Look for Plasmodium parasites.
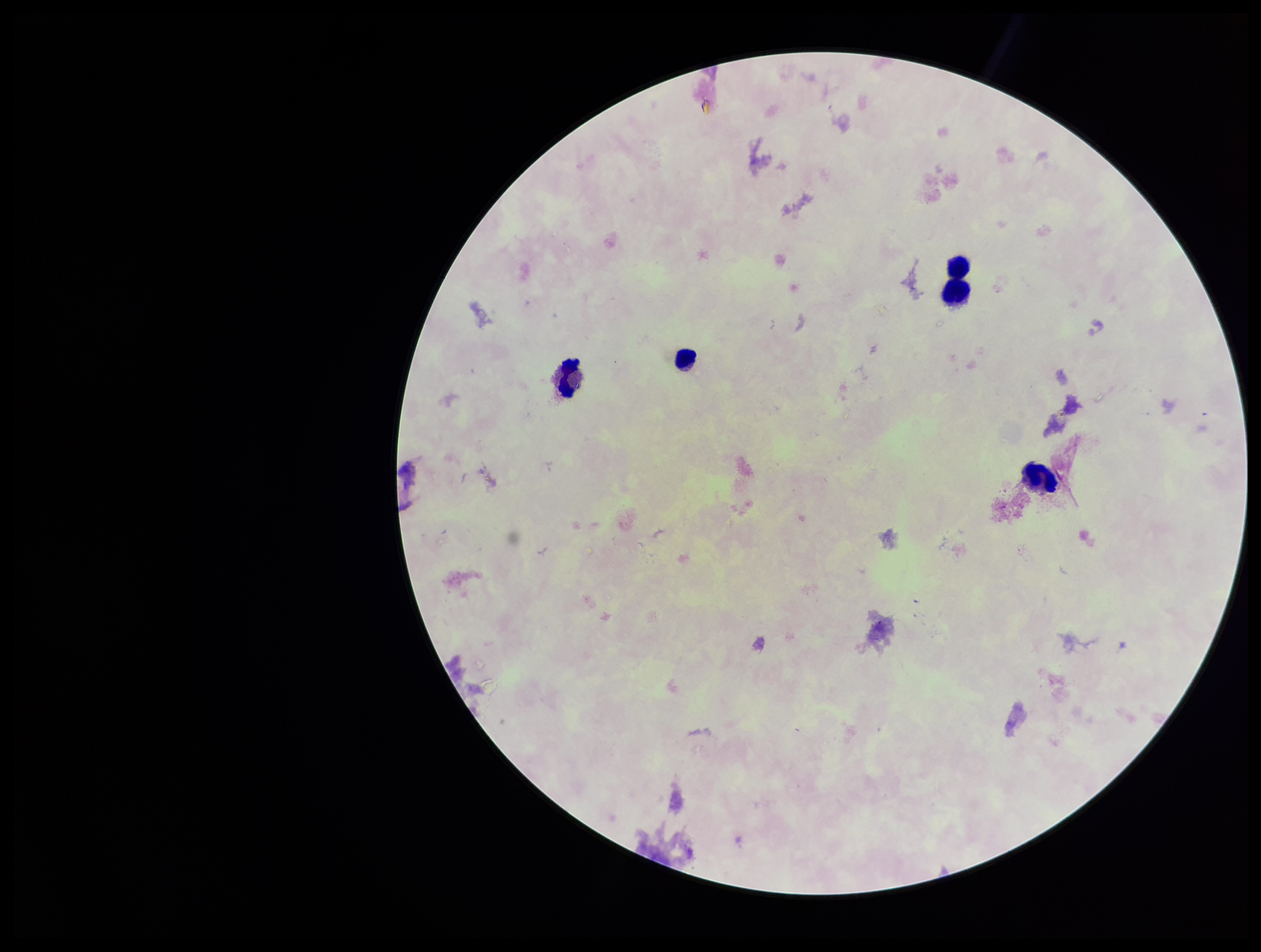
None seen.

Summary:
  - Leukocyte count: 4
  - Parasite count: 0
  - Patient malaria status: negative
  - Capture: smartphone photograph through the microscope eyepiece
  - Field of view: single
  - Preparation: thick smear
  - Stain: Giemsa
  - Image size: 1261×952 pixels